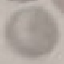

{
  "result": "negative for malaria parasites",
  "image_type": "cell patch, automatically extracted from a larger field of view and resized to 64 × 64 pixels",
  "stain": "Giemsa",
  "capture": "smartphone camera at the microscope eyepiece",
  "preparation": "thin blood smear"
}